Give the position of every malaria parasite.
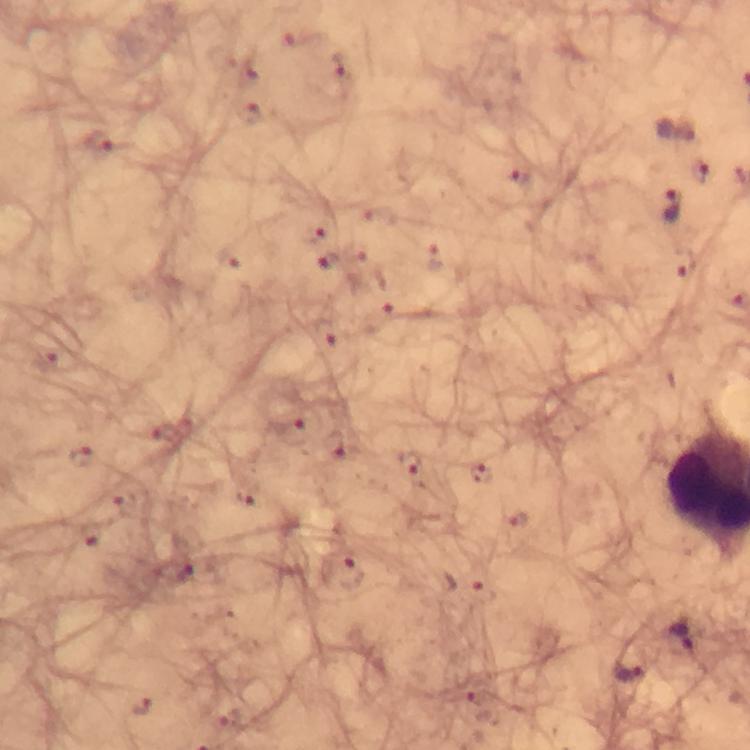

Approximate centers as {x, y} in pixels.
Malaria parasites: {339, 69}, {250, 112}, {677, 127}, {98, 144}, {698, 170}, {520, 176}, {672, 204}, {315, 231}, {329, 260}, {51, 359}, {295, 432}, {334, 446}, {80, 458}, {408, 464}, {479, 473}, {245, 493}, {123, 503}, {520, 521}, {91, 534}, {174, 571}, {343, 572}, {480, 593}, {687, 639}, {631, 671}, {141, 705}.

Summary:
  - Image size: 750×750 pixels
  - Context: from a diagnostic examination for malaria
  - Stain: Giemsa
  - Capture: smartphone mounted on the microscope
  - Cropped from: a single field of view
  - Immersion oil: used
  - Magnification: 100x
  - Preparation: thick smear